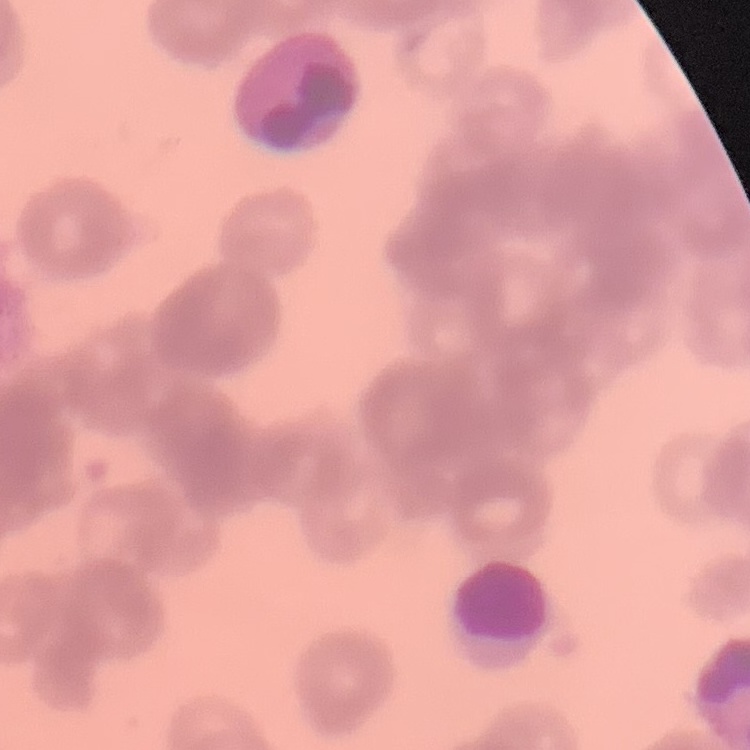
red blood cell morphology = rouleaux formation
stain = Field's or Giemsa
preparation = thin blood smear
image type = square crop of a larger photomicrograph